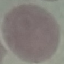 Malaria status: uninfected. Acquired by smartphone through the microscope eyepiece. Automatically extracted cell patch, resized to 64 × 64 pixels. Thin smear of blood. Giemsa stain.